Assess this cell for malaria.
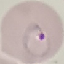
It is parasitized.

Summary:
  - Image type: automatically extracted cell patch, resized to 64 × 64 pixels
  - Capture: smartphone camera at the microscope eyepiece
  - Stain: Giemsa
  - Preparation: thin blood smear